Evaluate for malaria.
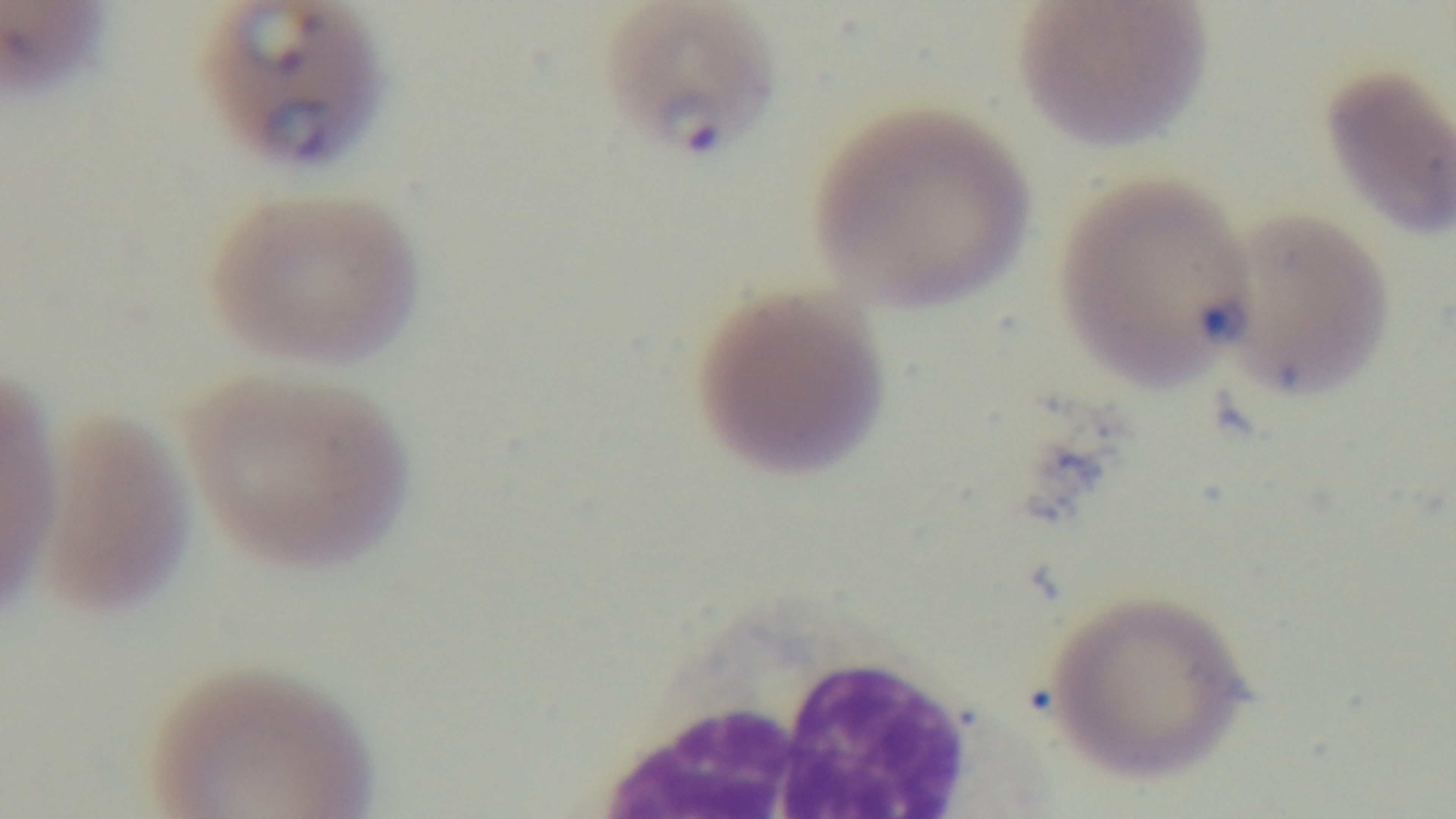

Positive.

stain = Giemsa
field of view = single
capture = mounted 4K digital camera
objective = 100x oil immersion
preparation = thin
modality = light microscopy